Assess this cell for malaria.
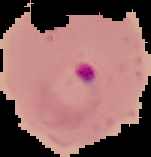
Parasitized.

From a thin blood smear. Image is 151×157 pixels. The area outside the segmented cell region is set to black.